Comment on the morphology of the erythrocytes.
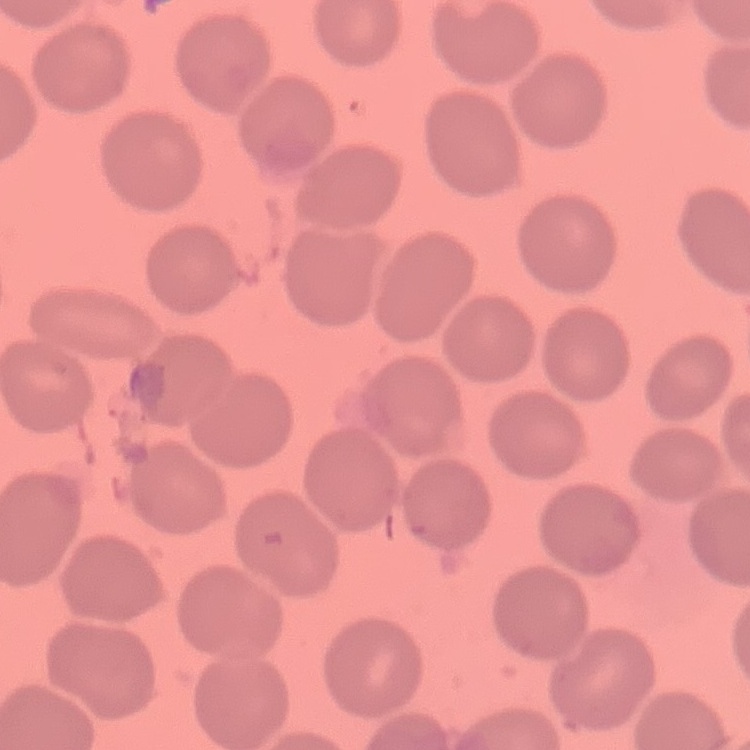
They show no rouleaux formation.

stain: Field's or Giemsa
image_type: one tile cut from a larger photomicrograph
preparation: thin blood smear